Classify this cell by malaria status.
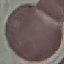

It is uninfected.

Cell patch, automatically extracted from a larger field of view and resized to 64 × 64 pixels. Giemsa-stained preparation. Thin blood film. Photographed with a smartphone camera at the microscope eyepiece.